Comment on the morphology of the red blood cells.
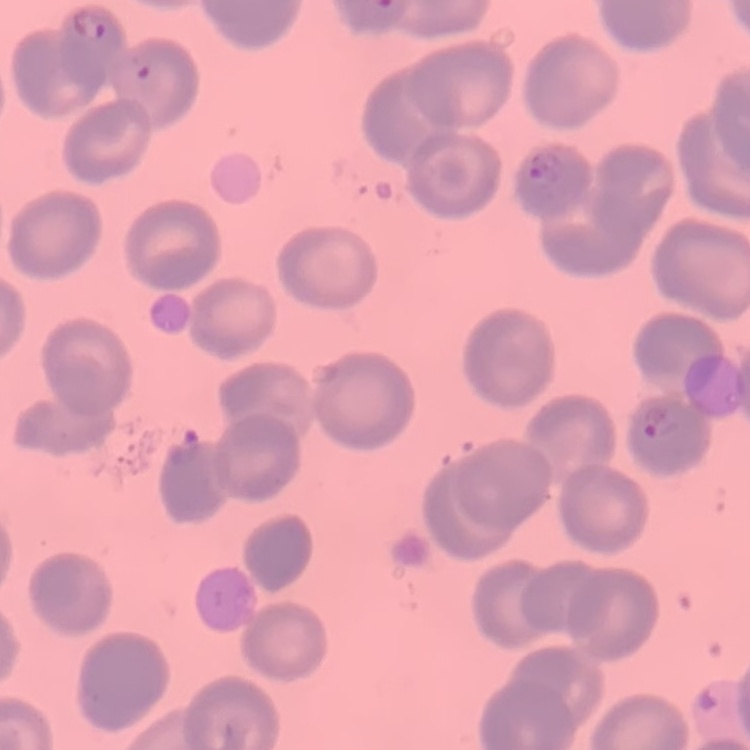

No rouleaux formation.

Summary:
  - Image type: square crop of a larger photomicrograph
  - Preparation: thin blood smear
  - Stain: Field's or Giemsa